Classify this cell by malaria status.
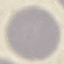
Uninfected.

preparation = thin smear
capture = smartphone through the microscope eyepiece
stain = Giemsa
image type = cell patch, automatically extracted from a larger field of view and resized to 64 × 64 pixels